Identify the cell.
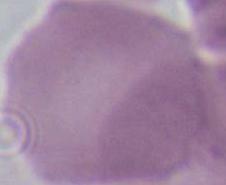

This is an erythrocyte.

Summary:
  - Modality: micrograph
  - Magnification: 1000x